Comment on the morphology of the erythrocytes.
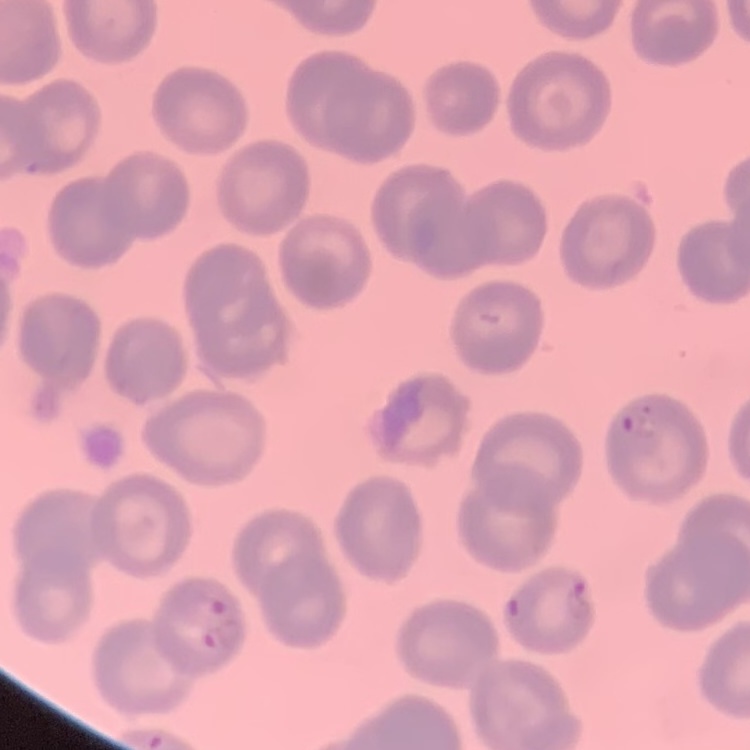

No rouleaux formation.

{
  "stain": "Field's or Giemsa",
  "image_type": "square crop of a larger photomicrograph",
  "preparation": "thin blood smear"
}